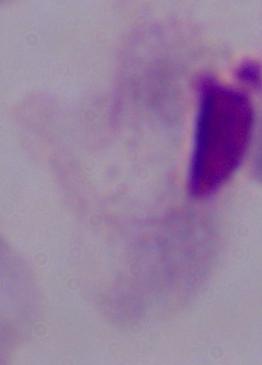

Captured at 1000x magnification. Photomicrograph. A trichomonad is seen.